Point out each malaria parasite.
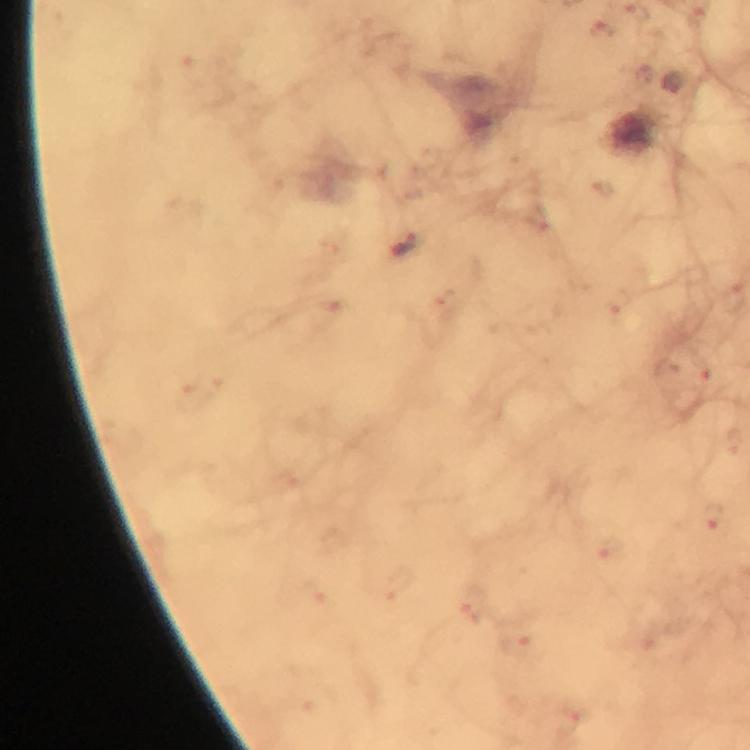

Approximate centers as [x, y] in pixels.
Malaria parasites: [404, 243].

Summary:
  - Preparation: thick blood smear
  - Cropped from: one field of view
  - Capture: smartphone mounted on the microscope
  - Stain: Giemsa
  - Immersion oil: applied
  - Context: from a diagnostic examination for malaria
  - Magnification: 100x
  - Image size: 750×750 pixels